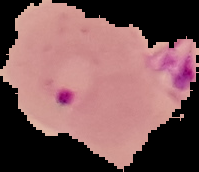 The area outside the segmented cell region is set to black. From a thin blood film. Result: malaria parasites detected. Image is 199×172 pixels.